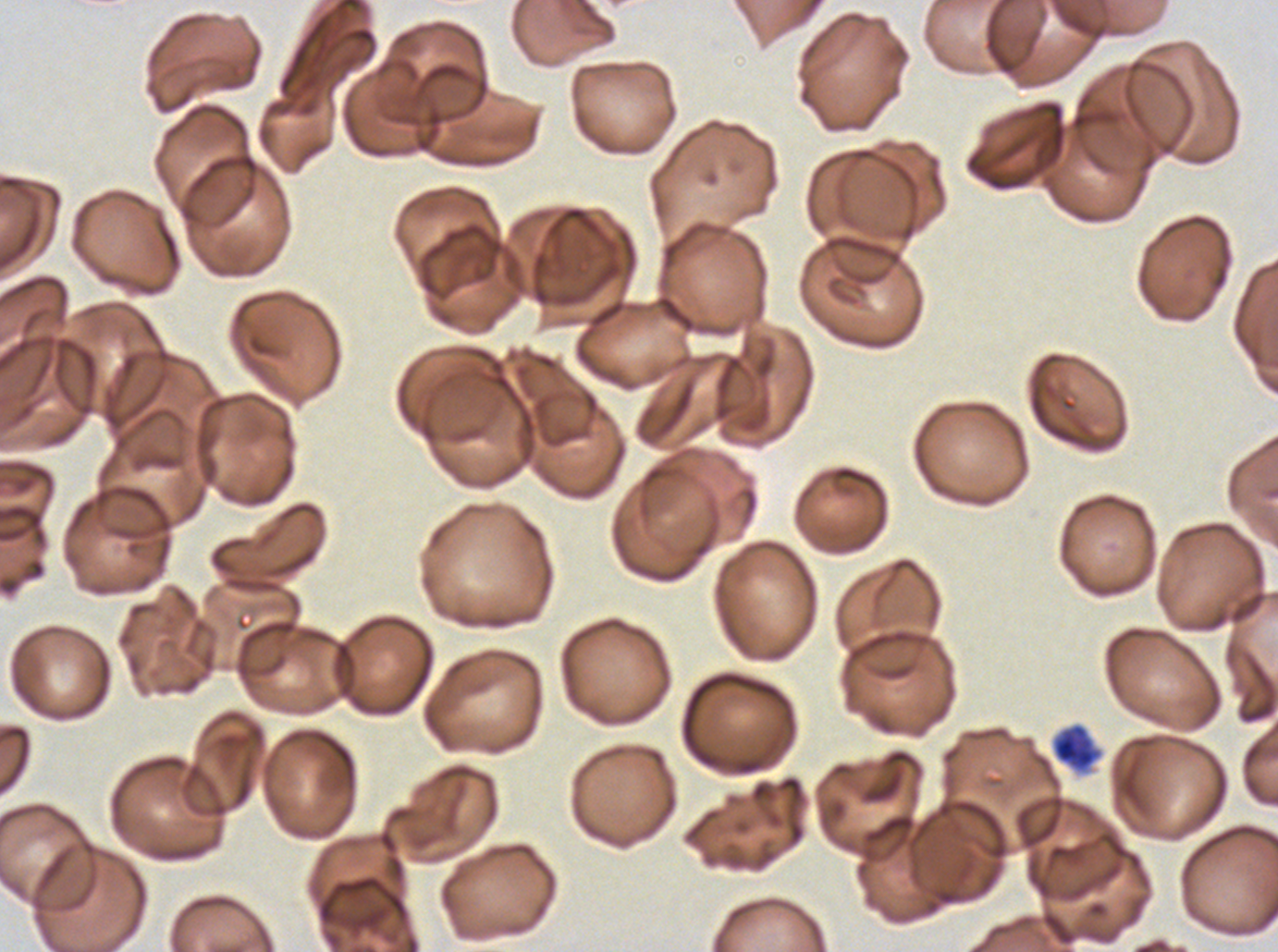

Approximate bounding rectangles given as corner coordinates in pixels from the top-left. Debris locations: (x1=1051, y1=723, x2=1101, y2=773). Giemsa stain. Image is 1278×952 pixels. A sub-image separated from a larger composite. P. falciparum cultured ex vivo for 24 to 48 hours, from a patient in The Gambia. Thin blood smear.